Name the parasite shown.
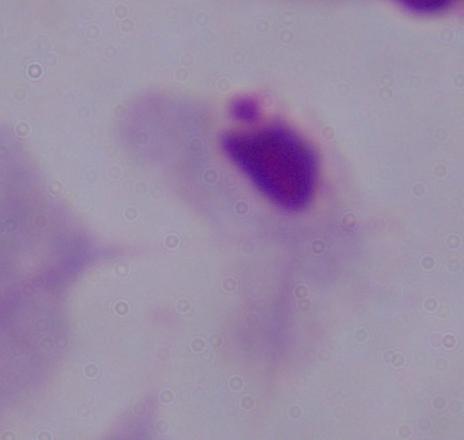
This is a trichomonad.

Captured at 1000x magnification. Micrograph.